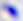
Summary:
  - Magnification: 400x
  - Modality: photomicrograph
  - Identification: Toxoplasma gondii